Classify this cell by malaria status.
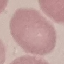

Uninfected.

preparation = thin blood film
image type = automatically extracted cell patch, resized to 64 × 64 pixels
capture = smartphone camera at the microscope eyepiece
stain = Giemsa